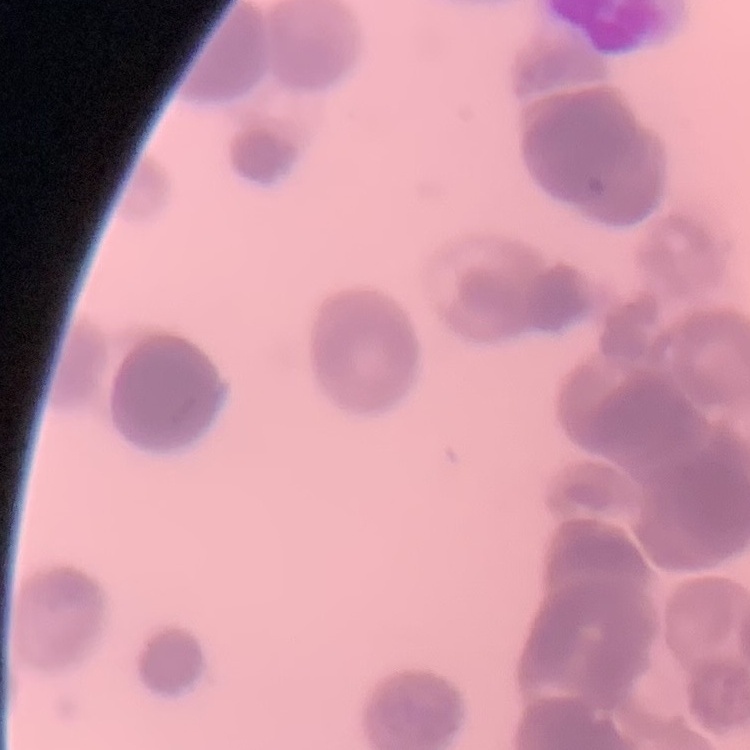
red blood cell morphology = rouleaux formation
stain = Field's or Giemsa
preparation = thin blood smear
image type = one tile cut from a larger photomicrograph